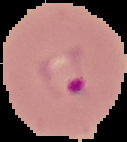
preparation: thin blood smear
image_size: 127×142 pixels
image_type: segmented cell region with the area outside set to black
malaria_status: parasitized